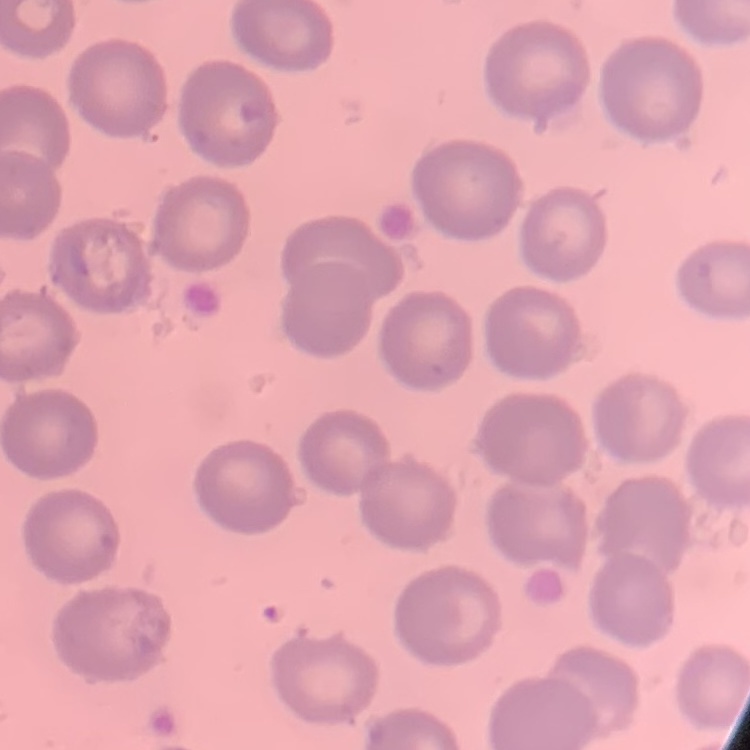

red blood cell morphology = no rouleaux formation
stain = Field's or Giemsa
preparation = thin blood smear
image type = one tile cut from a larger photomicrograph